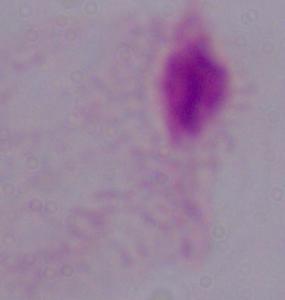

magnification = 1000x
modality = micrograph
identification = trichomonad